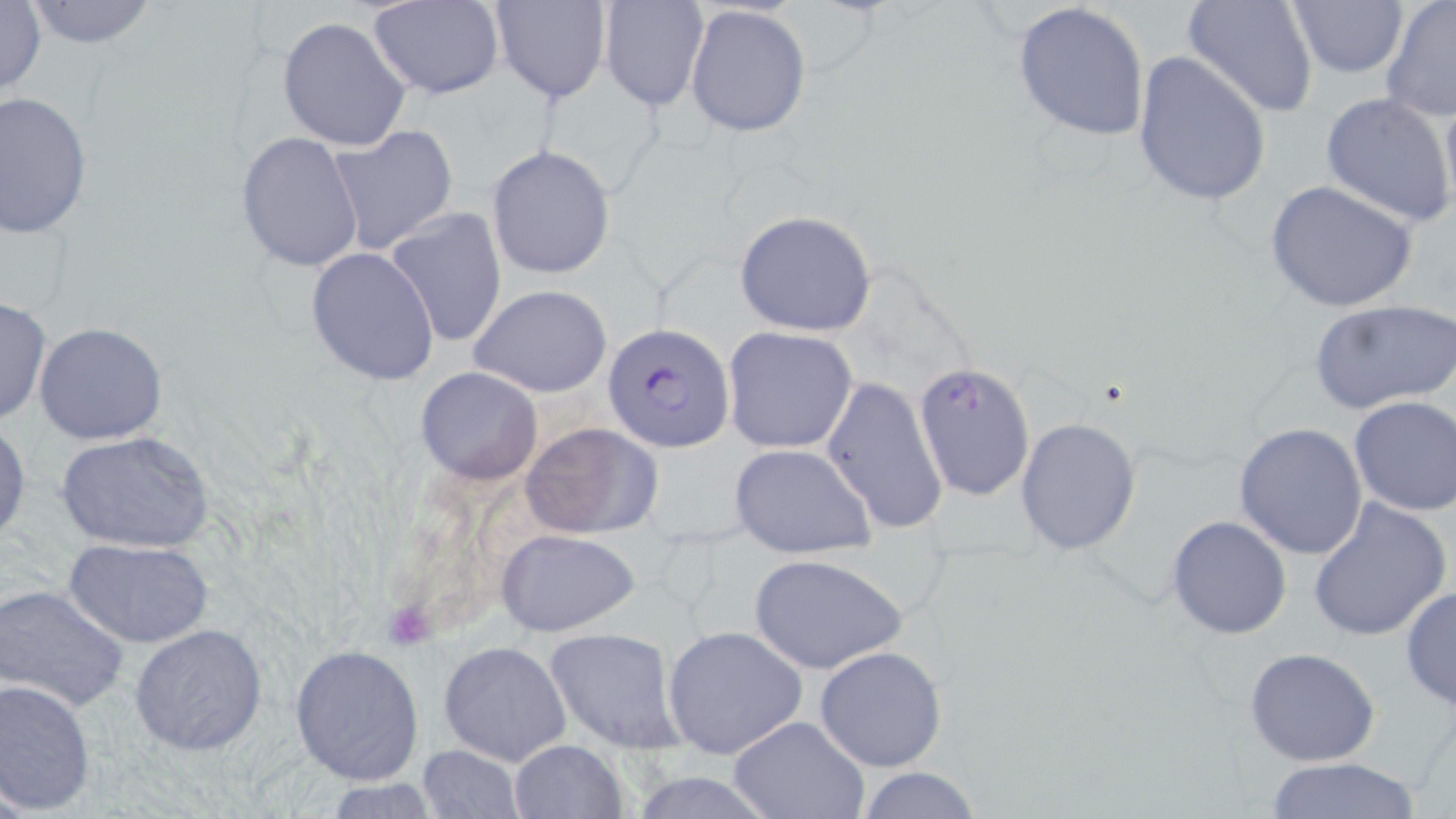 Approximate bounding boxes as (x1, y1, x2, y2) in pixels. Uninfected red blood cell locations: (0, 0, 47, 100), (22, 0, 160, 48), (598, 0, 709, 113), (1182, 0, 1318, 119), (1285, 0, 1408, 78), (1379, 0, 1456, 123), (367, 1, 505, 100), (488, 2, 610, 105), (1011, 2, 1151, 141), (685, 3, 813, 139), (277, 16, 412, 151), (1132, 51, 1272, 206), (1438, 89, 1456, 224), (0, 90, 94, 238), (1319, 91, 1456, 229), (326, 124, 460, 254), (237, 131, 365, 272), (487, 144, 615, 280), (1264, 180, 1418, 317), (385, 207, 509, 349), (733, 209, 880, 336), (305, 247, 440, 384), (469, 283, 612, 397), (0, 297, 51, 425), (1307, 298, 1456, 416), (34, 322, 167, 445), (722, 327, 858, 454), (416, 368, 542, 483), (822, 375, 947, 536), (1346, 395, 1455, 517), (1016, 417, 1141, 554), (0, 418, 30, 548), (519, 421, 665, 539), (1233, 422, 1369, 560), (56, 429, 215, 554), (729, 442, 876, 559), (1306, 497, 1453, 644), (1167, 516, 1293, 640), (496, 529, 640, 637), (62, 537, 215, 648), (749, 552, 908, 675), (1400, 584, 1456, 713), (0, 585, 130, 711), (131, 624, 268, 756), (661, 625, 808, 757), (544, 627, 688, 753), (438, 640, 573, 768), (289, 643, 425, 785), (814, 644, 948, 772), (1244, 646, 1382, 766), (0, 676, 98, 813), (725, 715, 870, 819), (507, 738, 628, 819), (415, 745, 527, 819), (1262, 757, 1424, 819), (854, 765, 986, 819), (628, 772, 782, 818). Plasmodium falciparum-infected red blood cell locations: (602, 323, 735, 452), (913, 360, 1033, 501). Slide-level diagnosis: Plasmodium falciparum. 1000x magnification. Optical microscopy. Image is 1456×819 pixels. Thin blood smear. One field of a larger specimen. May-Grünwald-Giemsa-stained preparation.